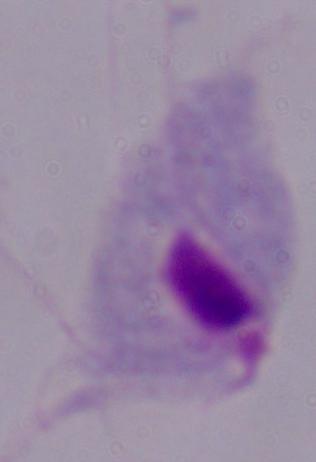
{
  "magnification": "1000x",
  "identification": "trichomonad",
  "modality": "photomicrograph"
}